Assess this cell for malaria.
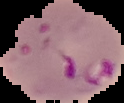
Parasitized.

image type = cell region segmented out of the field of view; surrounding area masked to black
image size = 124×103 pixels
preparation = thin blood smear